Classify this cell by malaria status.
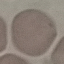

It is uninfected.

Summary:
  - Stain: Giemsa
  - Capture: smartphone through the microscope eyepiece
  - Image type: automatically extracted cell patch, resized to 64 × 64 pixels
  - Preparation: thin blood film